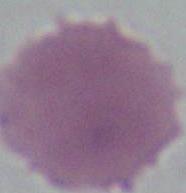

Micrograph. Captured at 1000x magnification. An erythrocyte is seen.